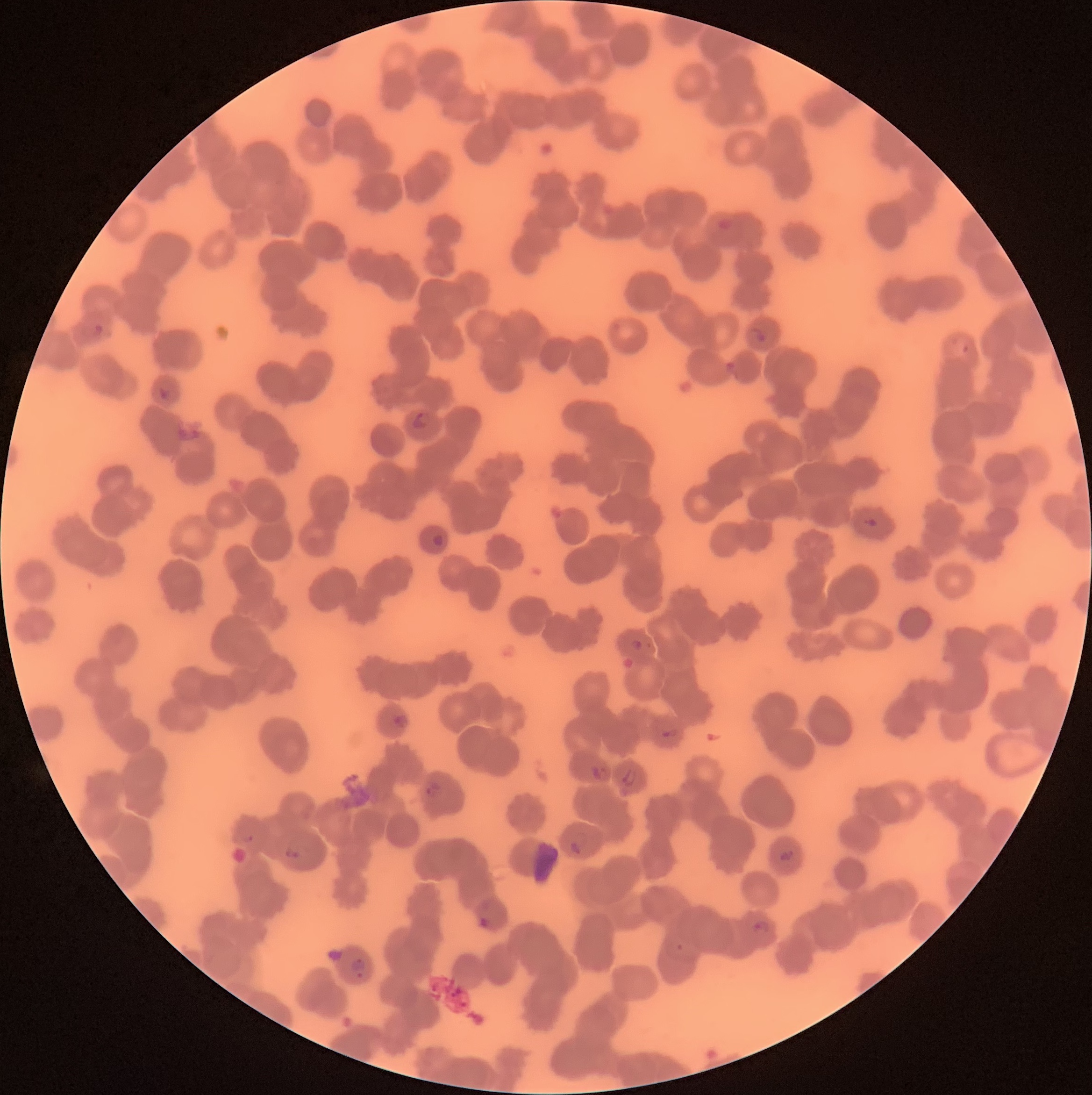

coordinate format = approximate bounding boxes as named x1/y1/x2/y2 corners in pixels
Plasmodium parasite locations = (x1=92, y1=323, x2=107, y2=336), (x1=747, y1=326, x2=767, y2=344), (x1=157, y1=387, x2=174, y2=400), (x1=411, y1=412, x2=432, y2=430), (x1=861, y1=514, x2=877, y2=528), (x1=430, y1=533, x2=444, y2=547), (x1=631, y1=639, x2=644, y2=652), (x1=393, y1=715, x2=408, y2=730), (x1=589, y1=764, x2=607, y2=780), (x1=622, y1=767, x2=637, y2=788), (x1=424, y1=781, x2=441, y2=799), (x1=568, y1=830, x2=588, y2=855), (x1=779, y1=847, x2=794, y2=864), (x1=751, y1=919, x2=771, y2=938), (x1=350, y1=958, x2=367, y2=980)
image size = 1092×1095 pixels
preparation = thin blood smear
modality = optical microscopy
red blood cell morphology = rouleaux formation